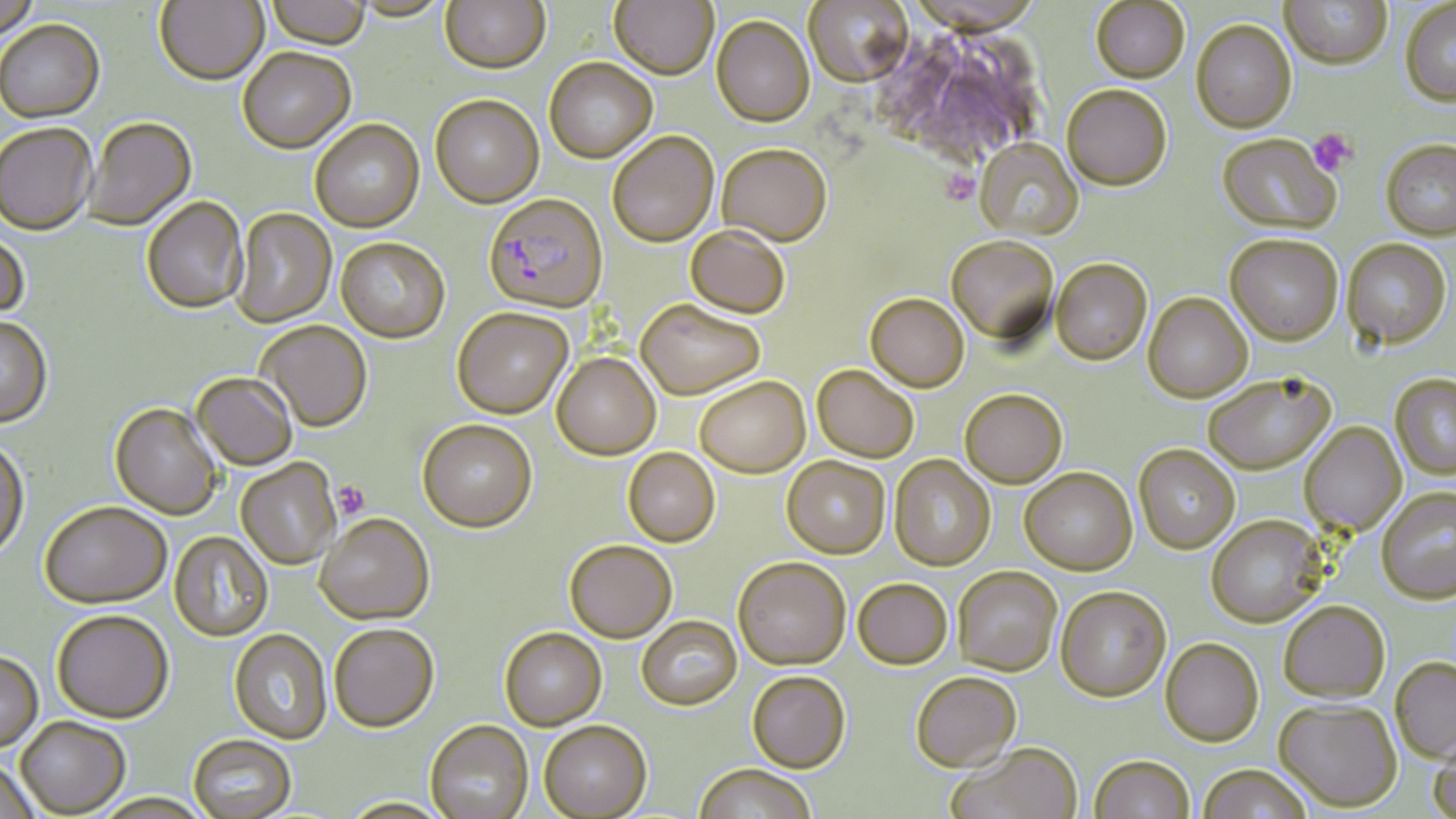

Approximate bounding boxes as (x1, y1, x2, y2) in pixels. Plasmodium falciparum-infected red blood cell locations: (483, 193, 608, 315). Uninfected red blood cell locations: (0, 0, 40, 42), (155, 0, 268, 85), (266, 0, 371, 49), (349, 0, 452, 22), (440, 0, 550, 73), (609, 0, 718, 81), (804, 0, 914, 88), (1280, 0, 1392, 73), (1090, 1, 1190, 86), (1400, 2, 1456, 108), (712, 16, 814, 128), (0, 19, 105, 123), (1191, 22, 1297, 136), (237, 47, 356, 153), (544, 58, 658, 162), (1062, 86, 1172, 193), (430, 93, 544, 207), (84, 118, 198, 231), (310, 119, 425, 232), (0, 124, 97, 236), (608, 131, 719, 247), (1216, 135, 1341, 238), (973, 140, 1084, 242), (1380, 142, 1456, 243), (717, 144, 832, 247), (141, 196, 248, 314), (232, 208, 336, 328), (685, 226, 790, 319), (0, 230, 29, 324), (945, 236, 1059, 347), (1225, 236, 1343, 347), (336, 237, 450, 343), (1341, 240, 1451, 351), (1050, 259, 1152, 365), (864, 293, 969, 393), (1143, 293, 1253, 403), (635, 299, 764, 400), (452, 307, 573, 418), (0, 316, 53, 428), (255, 320, 372, 433), (552, 353, 661, 461), (812, 365, 918, 463), (191, 372, 298, 470), (1390, 374, 1456, 481), (1203, 375, 1334, 475), (695, 377, 810, 479), (960, 389, 1067, 489), (110, 402, 222, 520), (418, 419, 537, 533), (1299, 422, 1406, 536), (0, 438, 29, 562), (1134, 444, 1240, 554), (623, 448, 720, 547), (889, 455, 996, 571), (782, 456, 891, 559), (236, 459, 342, 570), (1020, 468, 1137, 576), (1376, 487, 1455, 604), (39, 502, 171, 610), (315, 513, 435, 625), (1206, 515, 1327, 628), (169, 531, 273, 641), (564, 541, 677, 644), (733, 558, 850, 672), (953, 566, 1062, 676), (853, 579, 952, 671), (1055, 587, 1171, 702), (1279, 600, 1391, 702), (51, 611, 175, 725), (636, 617, 742, 711), (329, 624, 440, 733), (498, 628, 607, 731), (229, 629, 333, 745), (1160, 638, 1264, 747), (0, 653, 43, 754), (1390, 657, 1456, 764), (747, 672, 851, 774), (910, 672, 1021, 773), (1274, 698, 1402, 812), (15, 718, 130, 818), (425, 721, 533, 819), (538, 722, 652, 819), (188, 735, 296, 818), (1428, 735, 1456, 818), (947, 744, 1083, 819), (1089, 754, 1195, 819), (0, 761, 41, 819), (1197, 764, 1313, 819), (693, 765, 817, 819), (92, 794, 214, 819). Platelet locations: (1309, 128, 1358, 176), (939, 168, 981, 206), (331, 481, 370, 519). Slide-level diagnosis: Plasmodium falciparum. 1000x magnification. May-Grünwald-Giemsa-stained preparation. Image is 1456×819 pixels. Light microscopy. Single field of view. Thin blood smear.